Classify this cell by malaria status.
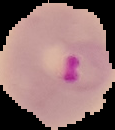

Parasitized.

Image is 115×130 pixels. From a thin blood smear. Cell region segmented out of the field of view; the surrounding area is masked to black.